Report the malaria status of this cell.
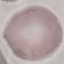
Uninfected.

preparation = thin smear
image type = cell patch, automatically extracted from a larger field of view and resized to 64 × 64 pixels
stain = Giemsa
capture = smartphone through the microscope eyepiece